Describe the morphology of the erythrocytes.
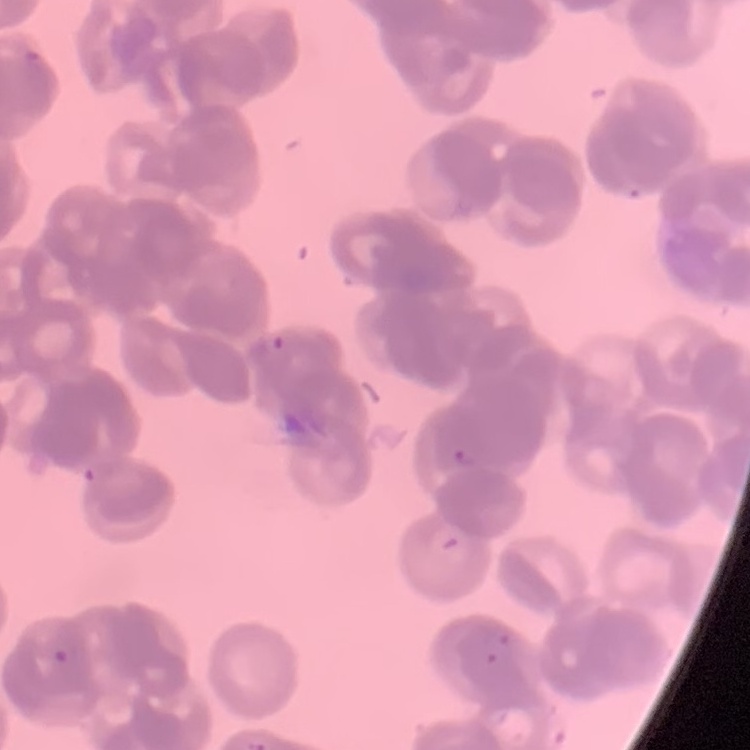

They show rouleaux formation.

Summary:
  - Stain: Field's or Giemsa
  - Image type: one tile cut from a larger photomicrograph
  - Preparation: thin peripheral smear